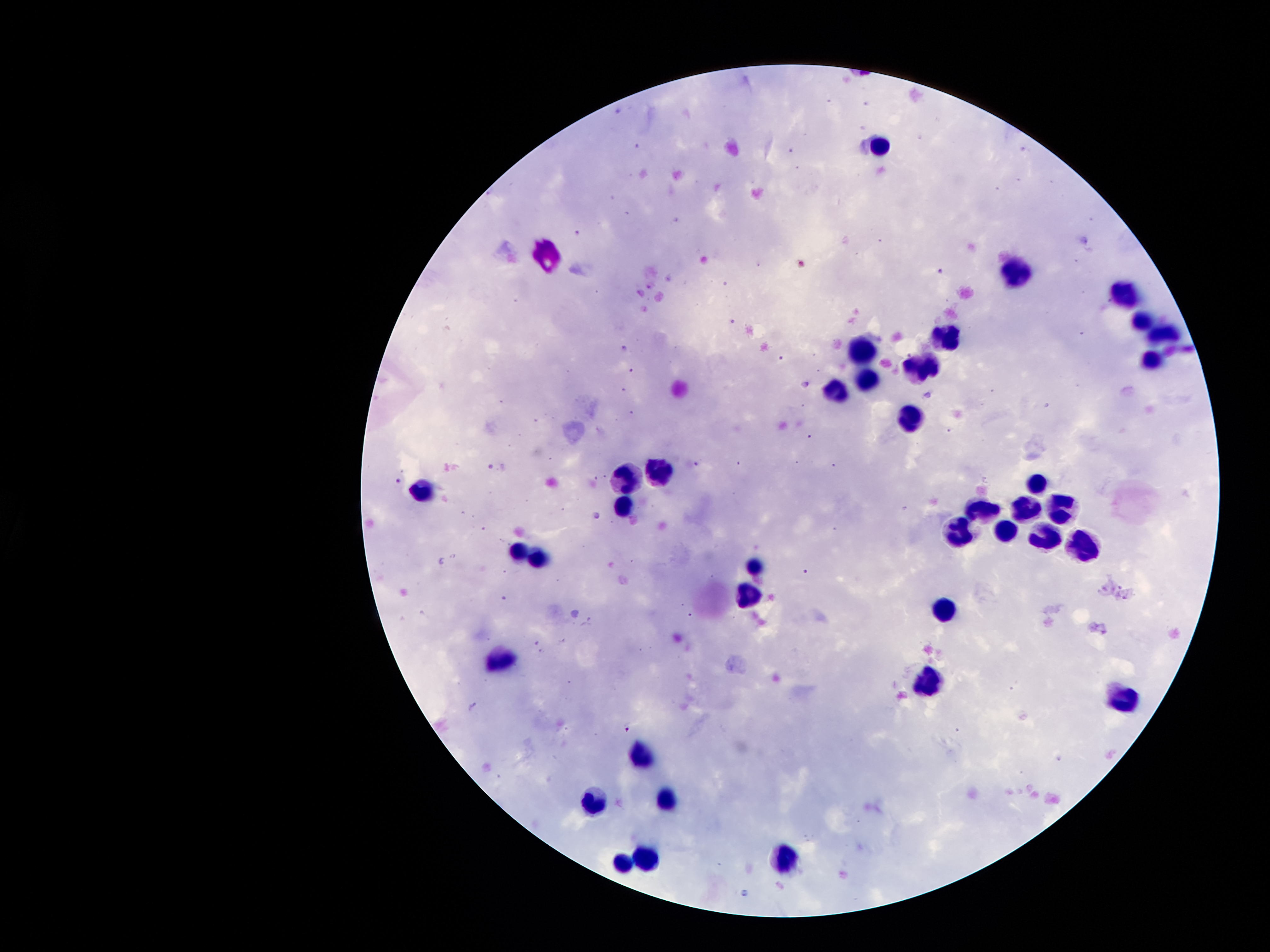

coordinate format = approximate centers as (x, y) in pixels
leukocyte locations = (879, 146), (547, 253), (1013, 265), (1126, 293), (1140, 319), (944, 333), (1164, 333), (863, 349), (1147, 357), (914, 364), (865, 381), (839, 388), (907, 416), (626, 467), (660, 470), (1036, 479), (419, 484), (622, 500), (980, 505), (1024, 505), (1059, 505), (1004, 523), (959, 530), (1041, 532), (520, 547), (1080, 547), (539, 553), (755, 561), (753, 591), (944, 606), (494, 666), (931, 673), (1126, 700), (641, 759), (667, 796), (588, 802), (648, 854), (784, 858), (618, 866)
malaria parasite locations = (940, 271), (807, 383), (696, 464), (398, 480), (598, 516), (805, 572), (628, 728)
capture = smartphone camera through the microscope eyepiece
patient malaria status = infected with Plasmodium falciparum
image size = 1270×952 pixels
preparation = thick blood film
stain = Giemsa
magnification = 100x
field of view = single